Describe the morphology of the erythrocytes.
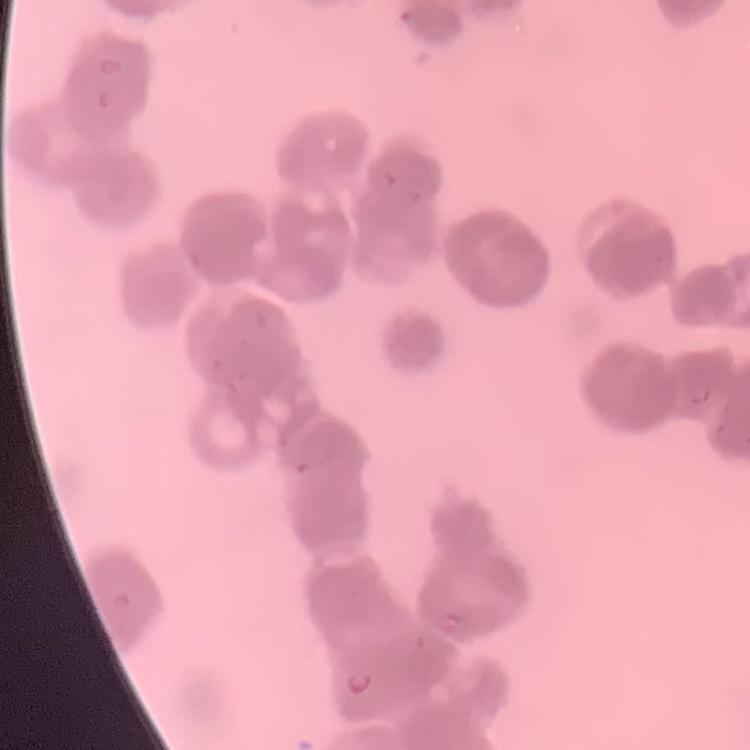
Rouleaux formation.

Summary:
  - Image type: one tile cut from a larger photomicrograph
  - Preparation: thin peripheral smear
  - Stain: Field's or Giemsa